Assess this cell for malaria.
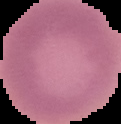
Uninfected.

image_type: cell region segmented out of the field of view; surrounding area masked to black
image_size: 121×124 pixels
preparation: thin blood smear